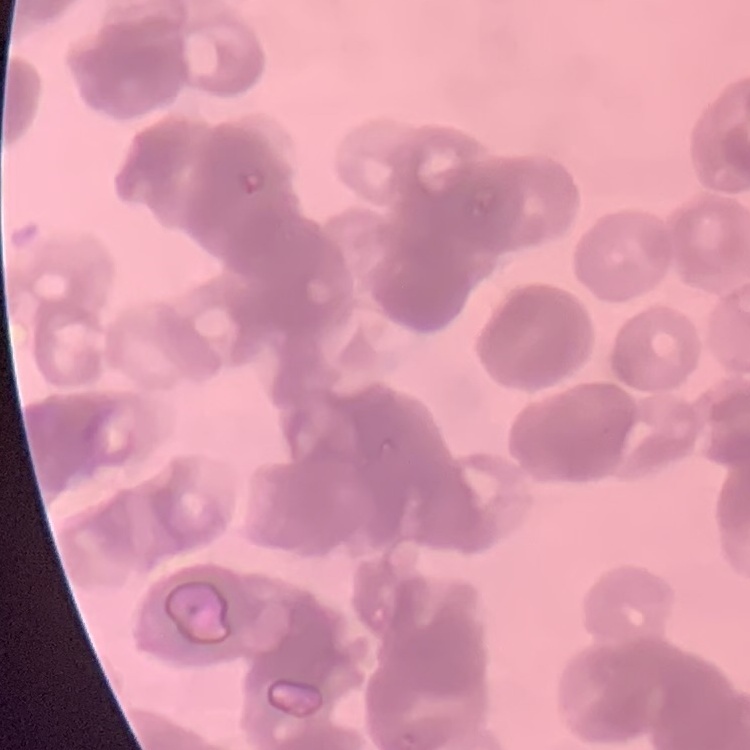

Summary:
  - Erythrocyte morphology: rouleaux formation
  - Stain: Field's or Giemsa
  - Preparation: thin blood smear
  - Image type: square crop of a larger photomicrograph